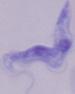

Summary:
  - Identification: trypanosome
  - Modality: photomicrograph
  - Magnification: 1000x